Name the blood parasite species.
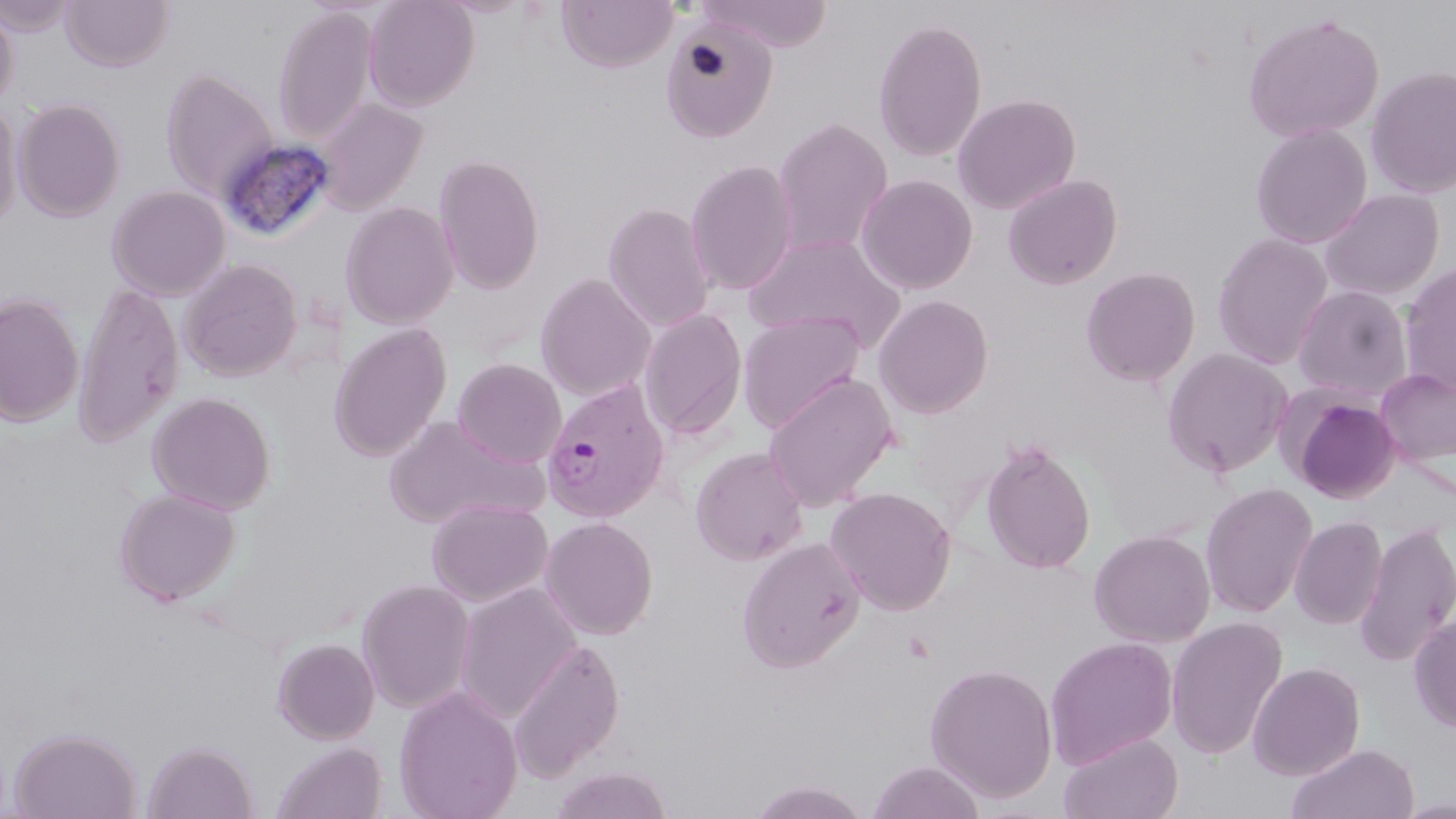

Plasmodium vivax.

Summary:
  - Coordinate format: approximate bounding boxes as [x1, y1, x2, y2] in pixels
  - Plasmodium vivax-infected red blood cell locations: [542, 375, 673, 523]
  - Uninfected red blood cell locations: [0, 0, 79, 37], [59, 0, 174, 71], [363, 0, 480, 111], [556, 0, 678, 72], [698, 0, 833, 52], [0, 6, 18, 106], [273, 6, 379, 145], [1241, 11, 1384, 143], [873, 16, 988, 163], [660, 17, 778, 143], [1365, 66, 1456, 198], [160, 67, 278, 202], [952, 93, 1081, 214], [0, 97, 24, 230], [13, 98, 126, 222], [314, 98, 428, 214], [772, 117, 893, 257], [1250, 123, 1373, 248], [432, 153, 545, 294], [685, 160, 799, 296], [856, 173, 977, 294], [1002, 173, 1123, 289], [106, 185, 231, 300], [1319, 189, 1444, 301], [340, 201, 459, 328], [603, 202, 715, 332], [1212, 232, 1334, 370], [743, 233, 906, 350], [179, 259, 303, 381], [1399, 263, 1456, 399], [1080, 267, 1200, 385], [535, 273, 655, 401], [72, 281, 183, 448], [1292, 284, 1413, 403], [0, 292, 84, 427], [873, 294, 994, 419], [639, 308, 747, 439], [737, 310, 867, 432], [329, 323, 452, 461], [1162, 347, 1294, 477], [452, 358, 567, 467], [1374, 367, 1456, 465], [763, 372, 899, 511], [1285, 390, 1402, 504], [146, 391, 276, 514], [384, 415, 547, 528], [979, 439, 1096, 575], [690, 445, 809, 566], [1200, 483, 1318, 619], [826, 486, 957, 615], [113, 487, 242, 606], [427, 498, 552, 607], [539, 516, 658, 639], [1290, 516, 1387, 629], [1355, 520, 1456, 668], [1088, 529, 1216, 648], [736, 537, 866, 672], [356, 578, 475, 713], [454, 582, 582, 722], [1408, 613, 1456, 733], [1165, 616, 1287, 759], [1045, 636, 1178, 769], [272, 637, 380, 744], [508, 637, 625, 782], [924, 661, 1059, 803], [1247, 662, 1365, 780], [393, 685, 523, 819], [8, 726, 142, 819], [1058, 732, 1183, 819], [143, 740, 258, 819], [271, 741, 387, 819], [1286, 743, 1419, 819], [867, 760, 986, 819], [549, 766, 674, 819], [747, 779, 872, 818]
  - Stain: May-Grünwald-Giemsa
  - Preparation: thin blood smear
  - Image size: 1456×819 pixels
  - Modality: optical microscopy
  - Field of view: one of a larger specimen
  - Magnification: 1000x